State which parasite is depicted.
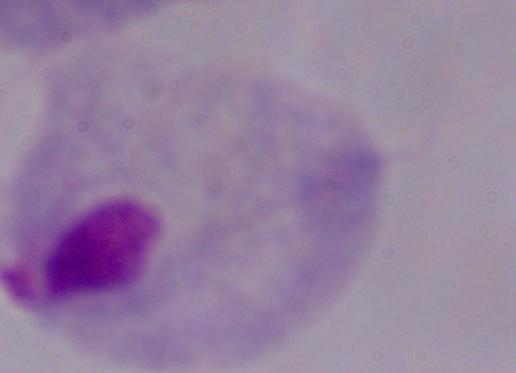

This is a trichomonad.

Summary:
  - Modality: photomicrograph
  - Magnification: 1000x